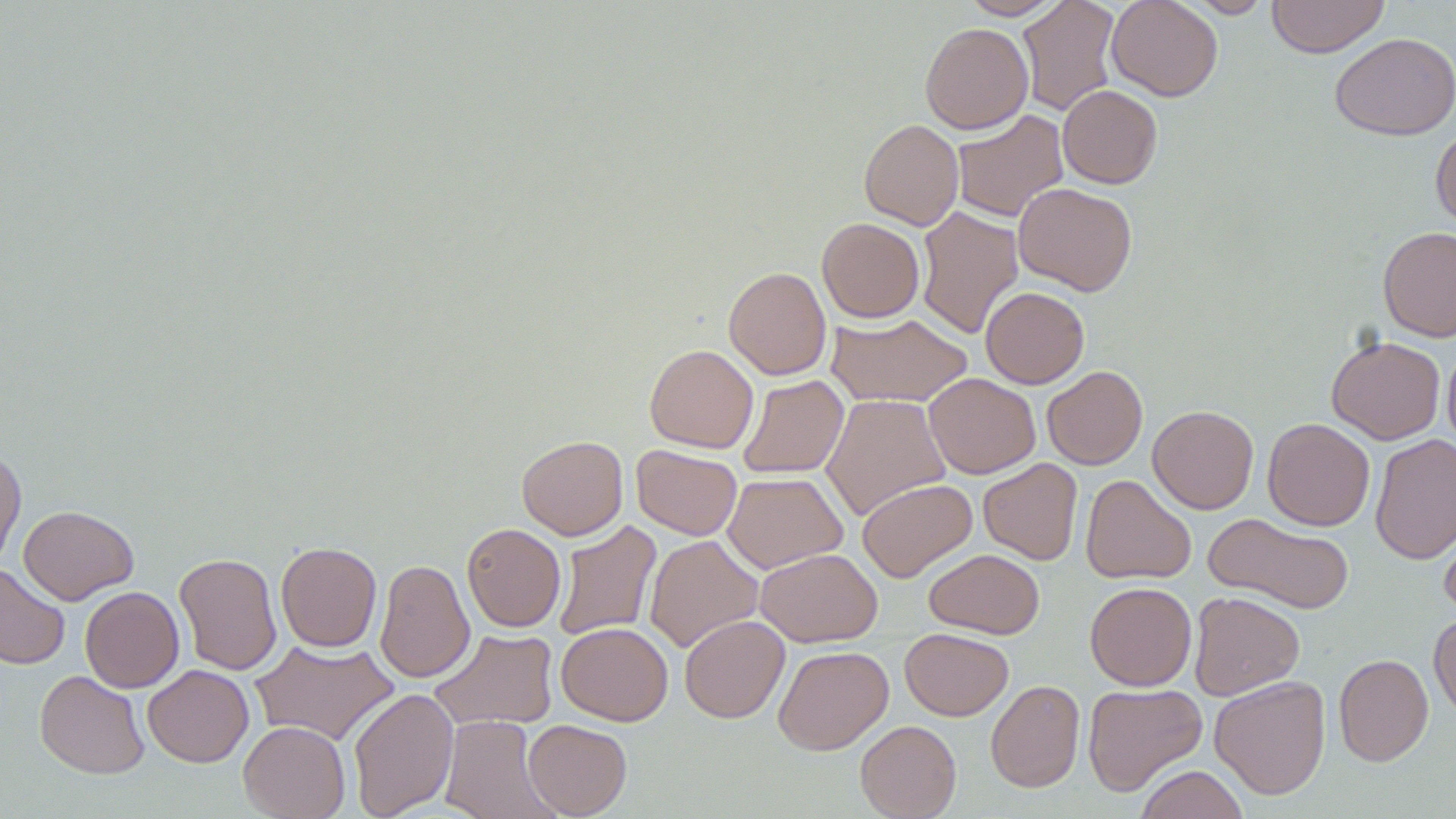
Summary:
  - Coordinate format: approximate bounding boxes as named x1/y1/x2/y2 corners in pixels
  - Uninfected red blood cell locations: (x1=958, y1=0, x2=1065, y2=20), (x1=1016, y1=0, x2=1121, y2=116), (x1=1106, y1=0, x2=1223, y2=101), (x1=1186, y1=0, x2=1273, y2=18), (x1=1266, y1=0, x2=1389, y2=57), (x1=920, y1=23, x2=1034, y2=134), (x1=1330, y1=32, x2=1455, y2=141), (x1=1057, y1=85, x2=1163, y2=188), (x1=951, y1=109, x2=1069, y2=223), (x1=859, y1=118, x2=964, y2=230), (x1=1430, y1=125, x2=1456, y2=230), (x1=1013, y1=182, x2=1138, y2=296), (x1=915, y1=205, x2=1024, y2=339), (x1=817, y1=217, x2=925, y2=323), (x1=1378, y1=226, x2=1456, y2=341), (x1=724, y1=266, x2=831, y2=380), (x1=980, y1=286, x2=1089, y2=388), (x1=825, y1=313, x2=973, y2=408), (x1=1327, y1=335, x2=1445, y2=444), (x1=644, y1=344, x2=758, y2=453), (x1=1442, y1=344, x2=1456, y2=449), (x1=1042, y1=365, x2=1147, y2=470), (x1=924, y1=372, x2=1041, y2=478), (x1=737, y1=375, x2=849, y2=478), (x1=821, y1=394, x2=951, y2=520), (x1=1147, y1=405, x2=1259, y2=514), (x1=1262, y1=418, x2=1375, y2=531), (x1=1370, y1=433, x2=1456, y2=564), (x1=516, y1=435, x2=628, y2=539), (x1=631, y1=445, x2=742, y2=540), (x1=0, y1=447, x2=26, y2=569), (x1=978, y1=458, x2=1083, y2=565), (x1=722, y1=472, x2=848, y2=573), (x1=1080, y1=474, x2=1196, y2=585), (x1=856, y1=478, x2=977, y2=582), (x1=18, y1=505, x2=138, y2=604), (x1=1438, y1=510, x2=1456, y2=619), (x1=1203, y1=513, x2=1356, y2=614), (x1=552, y1=521, x2=662, y2=642), (x1=462, y1=523, x2=566, y2=632), (x1=644, y1=535, x2=763, y2=653), (x1=275, y1=541, x2=382, y2=652), (x1=755, y1=548, x2=882, y2=647), (x1=924, y1=549, x2=1045, y2=638), (x1=173, y1=552, x2=282, y2=676), (x1=374, y1=558, x2=475, y2=684), (x1=0, y1=562, x2=70, y2=670), (x1=1084, y1=581, x2=1197, y2=691), (x1=80, y1=586, x2=184, y2=692), (x1=1188, y1=591, x2=1305, y2=700), (x1=1429, y1=612, x2=1456, y2=721), (x1=679, y1=615, x2=789, y2=723), (x1=556, y1=622, x2=673, y2=725), (x1=429, y1=628, x2=558, y2=731), (x1=900, y1=628, x2=1013, y2=720), (x1=250, y1=639, x2=398, y2=747), (x1=773, y1=645, x2=893, y2=755), (x1=1334, y1=653, x2=1433, y2=766), (x1=142, y1=665, x2=253, y2=767), (x1=34, y1=670, x2=150, y2=779), (x1=1209, y1=676, x2=1331, y2=799), (x1=986, y1=679, x2=1085, y2=793), (x1=1082, y1=683, x2=1207, y2=797), (x1=347, y1=687, x2=459, y2=818), (x1=440, y1=715, x2=558, y2=819), (x1=523, y1=719, x2=632, y2=818), (x1=855, y1=720, x2=961, y2=819), (x1=238, y1=721, x2=350, y2=819), (x1=1134, y1=765, x2=1249, y2=819)
  - Slide-level diagnosis: negative for blood parasites
  - Magnification: 1000x
  - Field of view: one of a larger specimen
  - Image size: 1456×819 pixels
  - Preparation: thin blood smear
  - Stain: May-Grünwald-Giemsa
  - Modality: optical microscopy